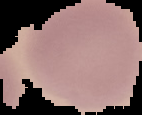

image_type: segmented cell region with the area outside set to black
image_size: 142×115 pixels
preparation: thin blood film
malaria_status: uninfected